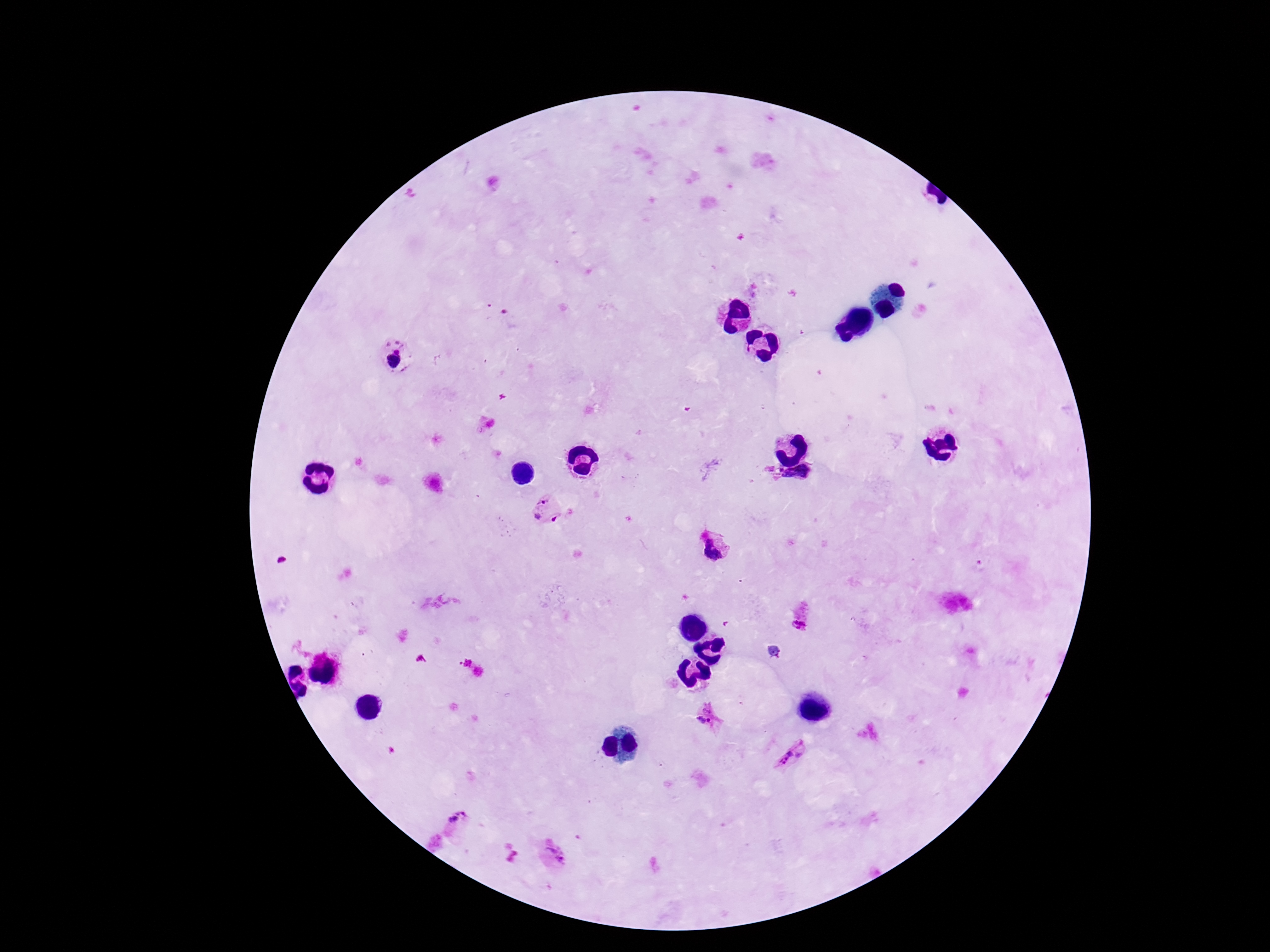

preparation = thick blood smear
magnification = 100x
capture = smartphone camera through the microscope eyepiece
stain = Giemsa
image size = 1270×952 pixels
patient malaria status = positive
field of view = single
Plasmodium parasite locations = approximate centers as {x, y} in pixels: {398, 343}, {389, 344}, {398, 351}, {393, 361}, {543, 500}, {537, 516}, {555, 519}, {711, 550}, {800, 622}, {706, 715}, {791, 759}, {457, 818}, {556, 852}